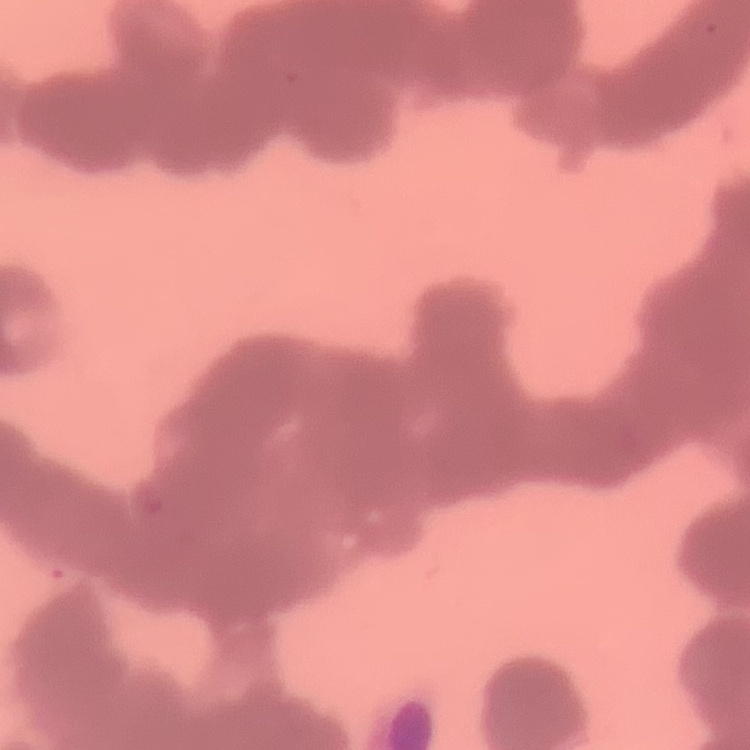
The red blood cells show rouleaux formation. Thin peripheral smear. Square crop of a larger photomicrograph. Field's or Giemsa stain.